Identify the parasite.
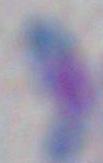
This is Toxoplasma gondii.

magnification = 1000x
modality = micrograph